Locate every Plasmodium falciparum-infected red blood cell.
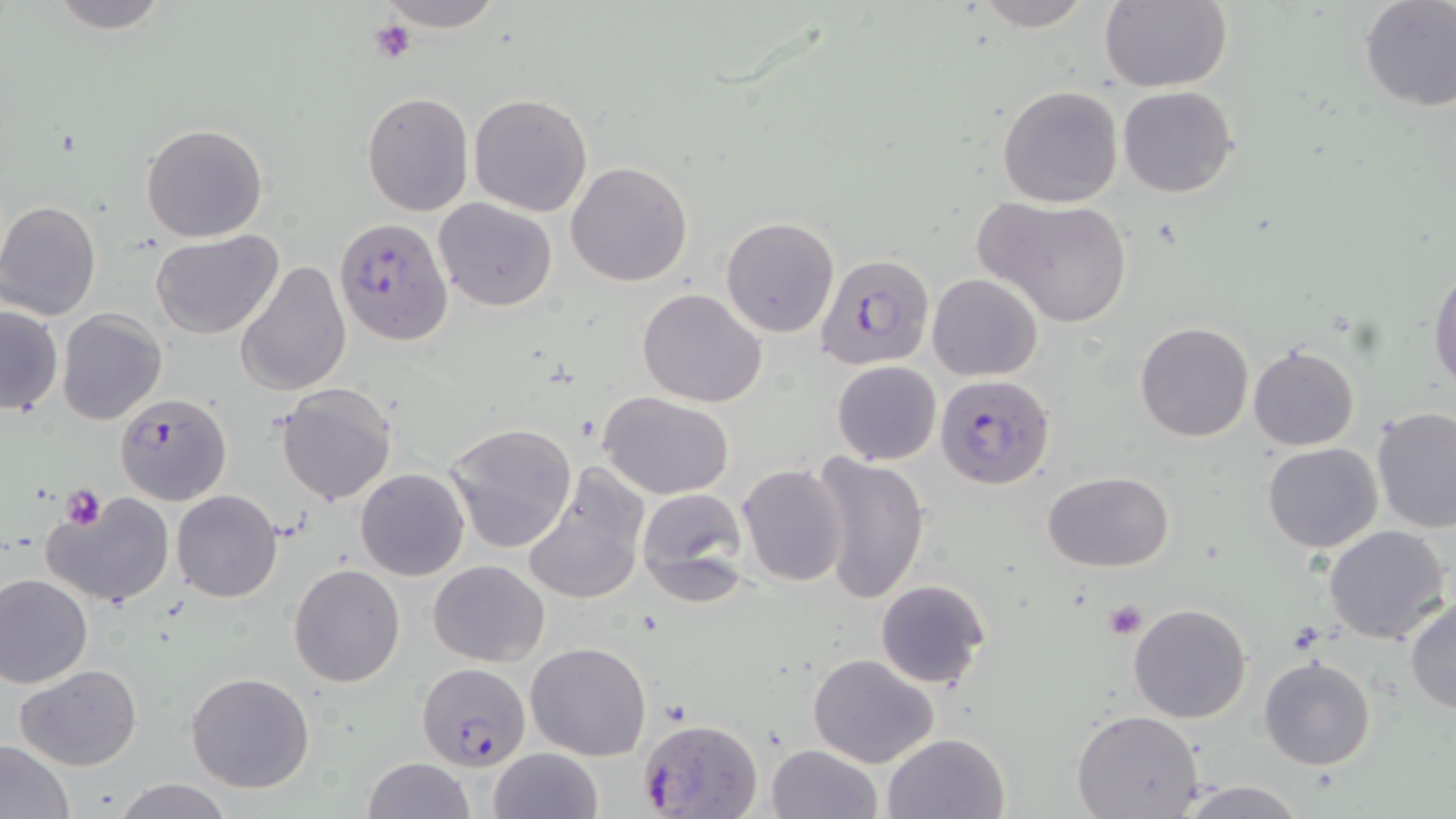
Approximate bounding boxes as (x1,y1)-(x2,y2) corner pairs in pixels.
Plasmodium falciparum-infected red blood cells: (333,216)-(454,348), (820,251)-(937,379), (934,373)-(1056,491), (113,394)-(233,505), (416,661)-(531,770), (637,718)-(762,818).

Platelet locations: (369,18)-(416,65), (61,485)-(107,529), (1103,601)-(1148,639). Uninfected red blood cell locations: (45,0)-(172,33), (375,0)-(506,30), (968,0)-(1094,32), (1358,0)-(1456,111), (1098,1)-(1232,92), (997,84)-(1124,208), (1117,86)-(1239,197), (361,93)-(473,215), (468,93)-(592,217), (140,123)-(269,242), (565,161)-(693,286), (976,194)-(1133,326), (434,197)-(559,311), (0,201)-(102,321), (720,216)-(840,339), (149,230)-(284,340), (237,258)-(352,398), (1429,263)-(1456,389), (927,273)-(1043,382), (636,287)-(767,407), (0,304)-(63,417), (57,310)-(167,426), (1134,321)-(1254,441), (1248,344)-(1360,452), (832,360)-(941,465), (275,383)-(398,504), (598,392)-(734,498), (1371,407)-(1456,533), (443,421)-(577,555), (1262,442)-(1383,552), (806,452)-(929,604), (521,463)-(650,606), (737,463)-(847,587), (355,468)-(470,581), (1042,470)-(1174,571), (635,486)-(752,605), (171,489)-(283,603), (44,493)-(177,610), (1323,525)-(1452,646), (429,559)-(549,667), (287,564)-(406,687), (0,574)-(92,689), (875,578)-(991,690), (1406,595)-(1456,715), (1128,603)-(1252,723), (525,641)-(652,761), (808,654)-(940,769), (1258,655)-(1376,770), (16,664)-(143,769), (185,671)-(315,793), (1071,707)-(1204,818), (882,731)-(1011,819), (0,740)-(79,819), (766,743)-(881,819), (488,748)-(603,819), (362,756)-(474,819), (113,777)-(232,818), (1173,779)-(1312,818). Slide-level diagnosis: Plasmodium falciparum. Single field of view. Image is 1456×819 pixels. Thin blood smear. Optical microscopy. May-Grünwald-Giemsa-stained preparation. Captured at 1000x magnification.